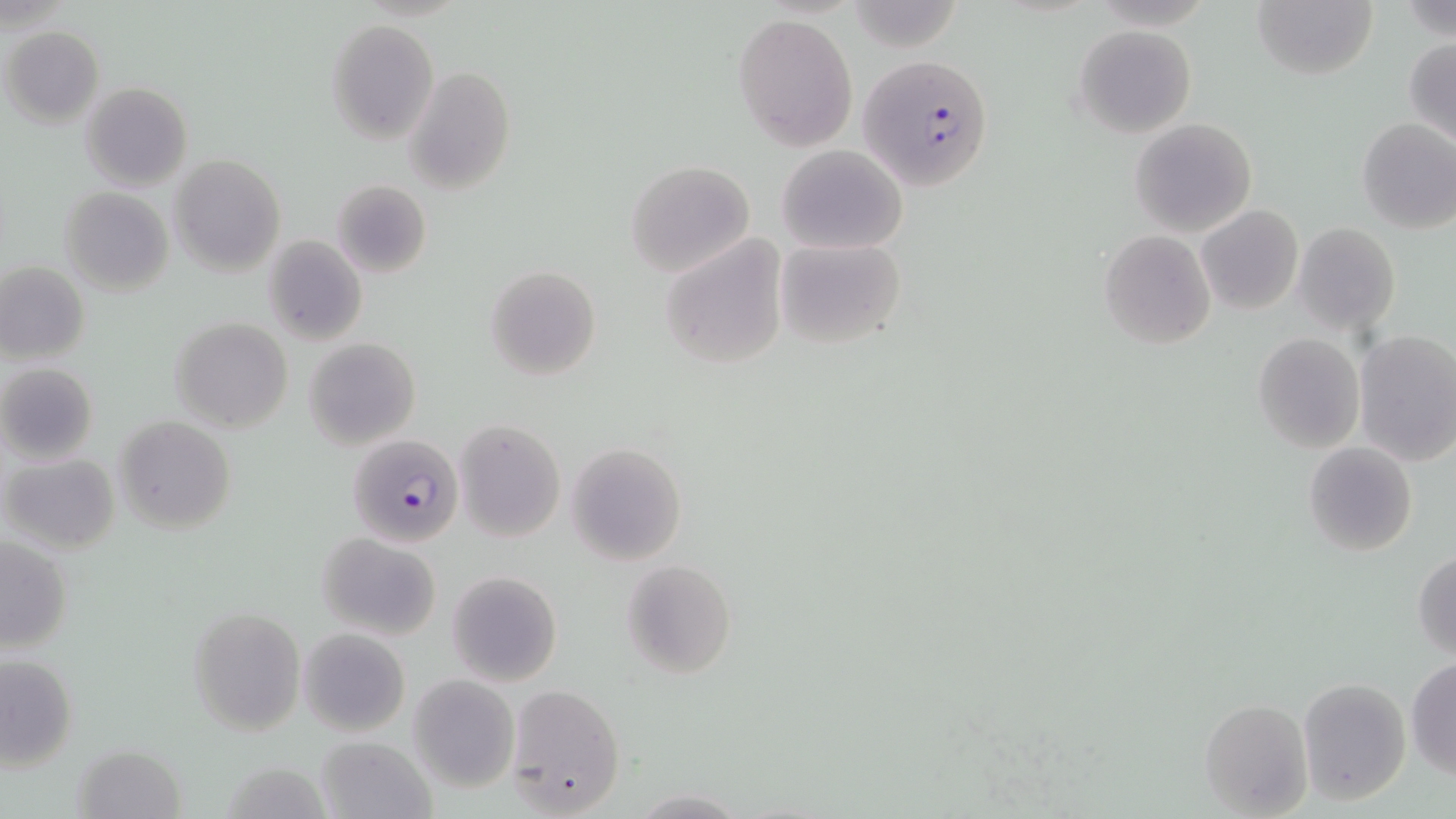
Summary:
  - Coordinate format: approximate bounding boxes as [x1, y1, x2, y2] in pixels
  - Uninfected red blood cell locations: [1253, 0, 1377, 80], [733, 13, 858, 151], [326, 19, 439, 143], [1074, 24, 1197, 137], [2, 27, 104, 128], [1404, 36, 1456, 145], [405, 66, 516, 193], [79, 82, 192, 191], [1356, 117, 1456, 234], [1128, 118, 1257, 238], [777, 143, 908, 254], [168, 154, 286, 277], [625, 160, 754, 277], [330, 180, 432, 278], [59, 186, 174, 296], [1196, 205, 1303, 314], [1292, 222, 1401, 335], [1099, 229, 1216, 349], [660, 234, 787, 368], [263, 235, 368, 346], [775, 237, 908, 349], [0, 261, 90, 365], [484, 265, 601, 381], [170, 317, 294, 433], [1354, 329, 1456, 464], [1252, 332, 1365, 454], [303, 337, 421, 451], [0, 363, 99, 464], [114, 416, 236, 534], [454, 418, 567, 542], [567, 442, 687, 566], [1302, 442, 1418, 556], [1, 453, 119, 555], [318, 532, 441, 640], [1, 536, 73, 654], [1412, 549, 1456, 659], [621, 559, 738, 679], [446, 569, 563, 687], [189, 608, 306, 737], [298, 628, 409, 736], [2, 651, 78, 771], [1406, 658, 1455, 779], [409, 676, 519, 793], [1298, 677, 1412, 804], [506, 685, 627, 815], [1201, 697, 1312, 817], [316, 736, 434, 819], [74, 743, 186, 819], [629, 790, 751, 818]
  - Plasmodium falciparum-infected red blood cell locations: [861, 55, 996, 192], [350, 438, 465, 547]
  - Slide-level diagnosis: Plasmodium falciparum
  - Stain: May-Grünwald-Giemsa
  - Field of view: single
  - Preparation: thin blood film
  - Magnification: 1000x
  - Image size: 1456×819 pixels
  - Modality: light microscopy